State the blood parasite species.
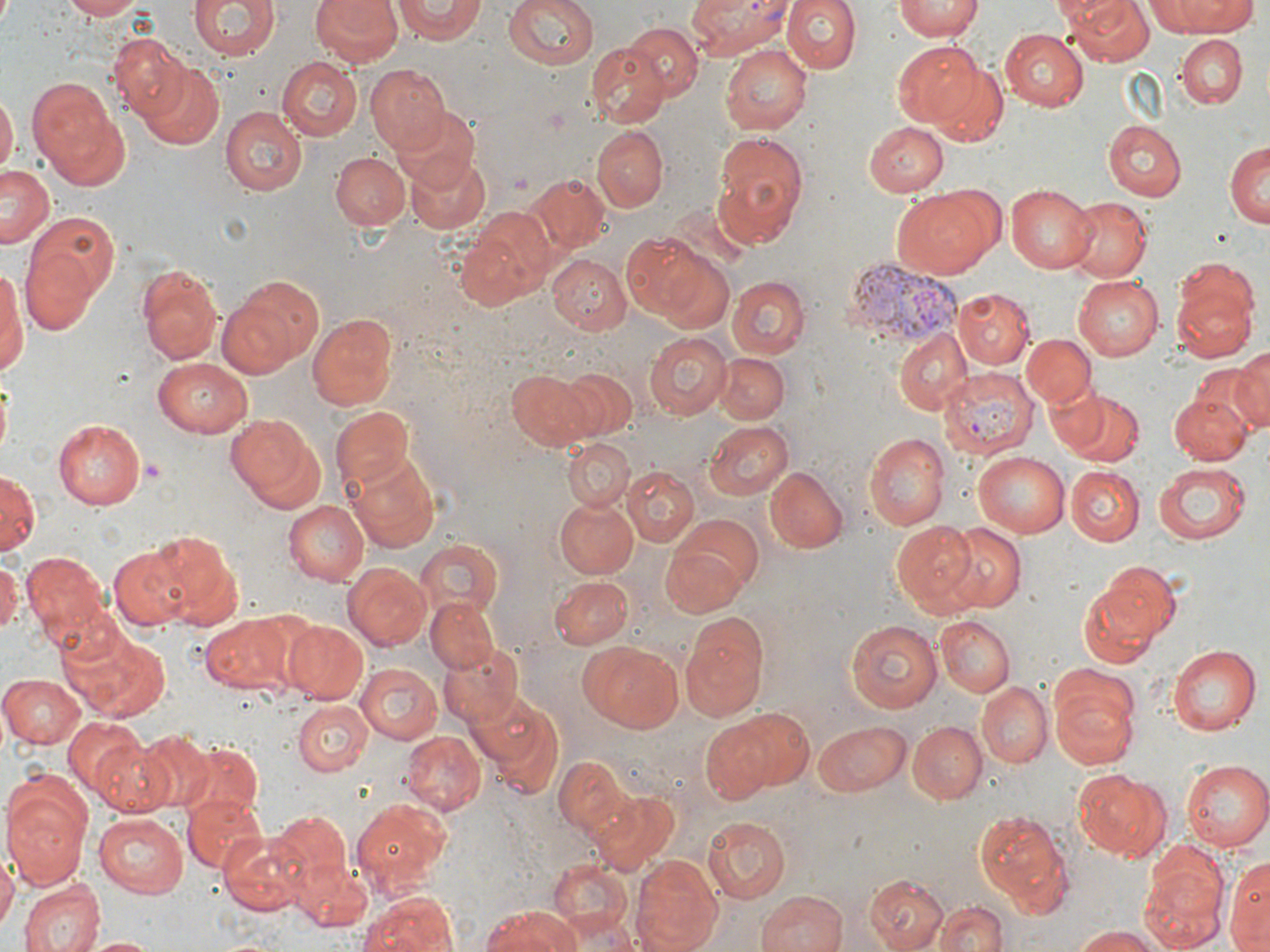

Plasmodium vivax.

Summary:
  - Coordinate format: approximate bounding boxes as [x1, y1, x2, y2] in pixels
  - Platelet locations: [137, 457, 167, 486]
  - Uninfected red blood cell locations: [62, 0, 145, 21], [191, 0, 279, 62], [311, 0, 405, 68], [503, 0, 599, 71], [780, 0, 860, 74], [895, 0, 982, 41], [1060, 0, 1155, 68], [1151, 0, 1258, 37], [393, 1, 486, 43], [618, 21, 703, 105], [999, 28, 1088, 109], [1176, 35, 1247, 107], [108, 36, 196, 123], [894, 39, 993, 132], [585, 44, 669, 128], [722, 44, 811, 132], [277, 57, 363, 140], [930, 61, 1010, 146], [139, 63, 224, 150], [365, 64, 449, 154], [26, 80, 117, 170], [0, 93, 16, 180], [40, 105, 134, 192], [220, 107, 306, 195], [393, 108, 480, 192], [865, 121, 949, 197], [1104, 122, 1187, 201], [592, 126, 668, 212], [712, 131, 809, 245], [1226, 142, 1270, 231], [332, 153, 410, 230], [406, 154, 490, 234], [1, 166, 56, 249], [524, 175, 609, 256], [1007, 184, 1098, 274], [892, 188, 999, 279], [1061, 198, 1149, 282], [456, 211, 556, 311], [26, 212, 119, 308], [623, 232, 718, 322], [21, 245, 100, 333], [549, 254, 633, 335], [0, 263, 26, 380], [137, 265, 223, 363], [1169, 272, 1257, 359], [1073, 275, 1164, 360], [220, 276, 326, 376], [728, 276, 810, 358], [950, 287, 1034, 370], [307, 311, 401, 413], [894, 329, 972, 415], [644, 332, 732, 419], [1022, 333, 1094, 408], [1231, 349, 1270, 434], [717, 353, 790, 425], [153, 359, 253, 438], [1196, 364, 1268, 447], [557, 368, 639, 442], [507, 369, 597, 449], [1042, 379, 1111, 455], [1171, 390, 1252, 466], [1063, 393, 1144, 469], [330, 406, 416, 494], [226, 413, 327, 514], [54, 420, 144, 508], [703, 420, 794, 501], [865, 433, 950, 531], [561, 437, 634, 513], [344, 452, 440, 551], [973, 452, 1069, 540], [1152, 464, 1251, 545], [622, 466, 699, 545], [1066, 466, 1145, 547], [766, 469, 848, 554], [0, 470, 39, 557], [554, 497, 638, 579], [283, 500, 369, 585], [675, 514, 764, 594], [891, 521, 980, 612], [945, 524, 1026, 613], [143, 530, 245, 628], [415, 537, 503, 620], [660, 541, 750, 616], [109, 545, 196, 630], [22, 552, 113, 641], [0, 560, 20, 637], [1088, 560, 1179, 648], [345, 563, 430, 649], [551, 575, 634, 650], [1076, 587, 1162, 668], [426, 597, 500, 674], [202, 613, 298, 694], [936, 615, 1015, 697], [845, 619, 944, 715], [280, 620, 369, 704], [679, 620, 768, 722], [62, 627, 172, 721], [581, 641, 685, 731], [439, 644, 525, 731], [1167, 644, 1259, 735], [355, 664, 442, 745], [0, 673, 84, 748], [1049, 679, 1140, 771], [976, 683, 1052, 767], [472, 696, 566, 798], [292, 700, 371, 775], [727, 706, 815, 790], [62, 718, 146, 799], [812, 719, 910, 795], [701, 721, 773, 803], [907, 721, 985, 804], [402, 731, 484, 814], [141, 733, 214, 809], [92, 738, 178, 816], [177, 742, 265, 818], [555, 755, 631, 836], [1182, 758, 1270, 850], [1072, 769, 1168, 861], [2, 777, 91, 890], [588, 790, 677, 876], [182, 794, 269, 876], [352, 796, 452, 889], [975, 808, 1075, 914], [268, 810, 353, 894], [93, 813, 188, 898], [702, 815, 792, 902], [218, 835, 305, 914], [0, 850, 16, 938], [630, 852, 723, 952], [1138, 853, 1227, 948], [1228, 854, 1269, 949], [293, 859, 372, 932], [545, 859, 634, 936], [865, 876, 949, 952], [19, 878, 104, 952], [757, 889, 847, 952], [359, 891, 456, 952], [933, 902, 1010, 952], [480, 908, 581, 952], [557, 912, 637, 952], [1071, 925, 1169, 951], [82, 936, 160, 952]
  - Plasmodium vivax-infected red blood cell locations: [686, 0, 792, 57], [843, 254, 961, 345], [941, 369, 1038, 458]
  - Magnification: 1000x
  - Preparation: thin blood film
  - Modality: optical microscopy
  - Image size: 1270×952 pixels
  - Stain: May-Grünwald-Giemsa
  - Field of view: single